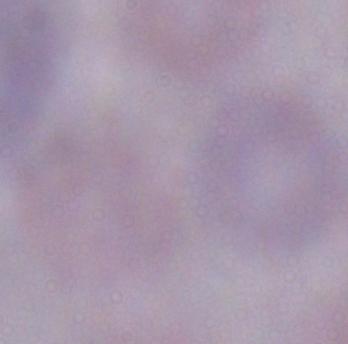

identification = trypanosome
modality = photomicrograph
magnification = 1000x